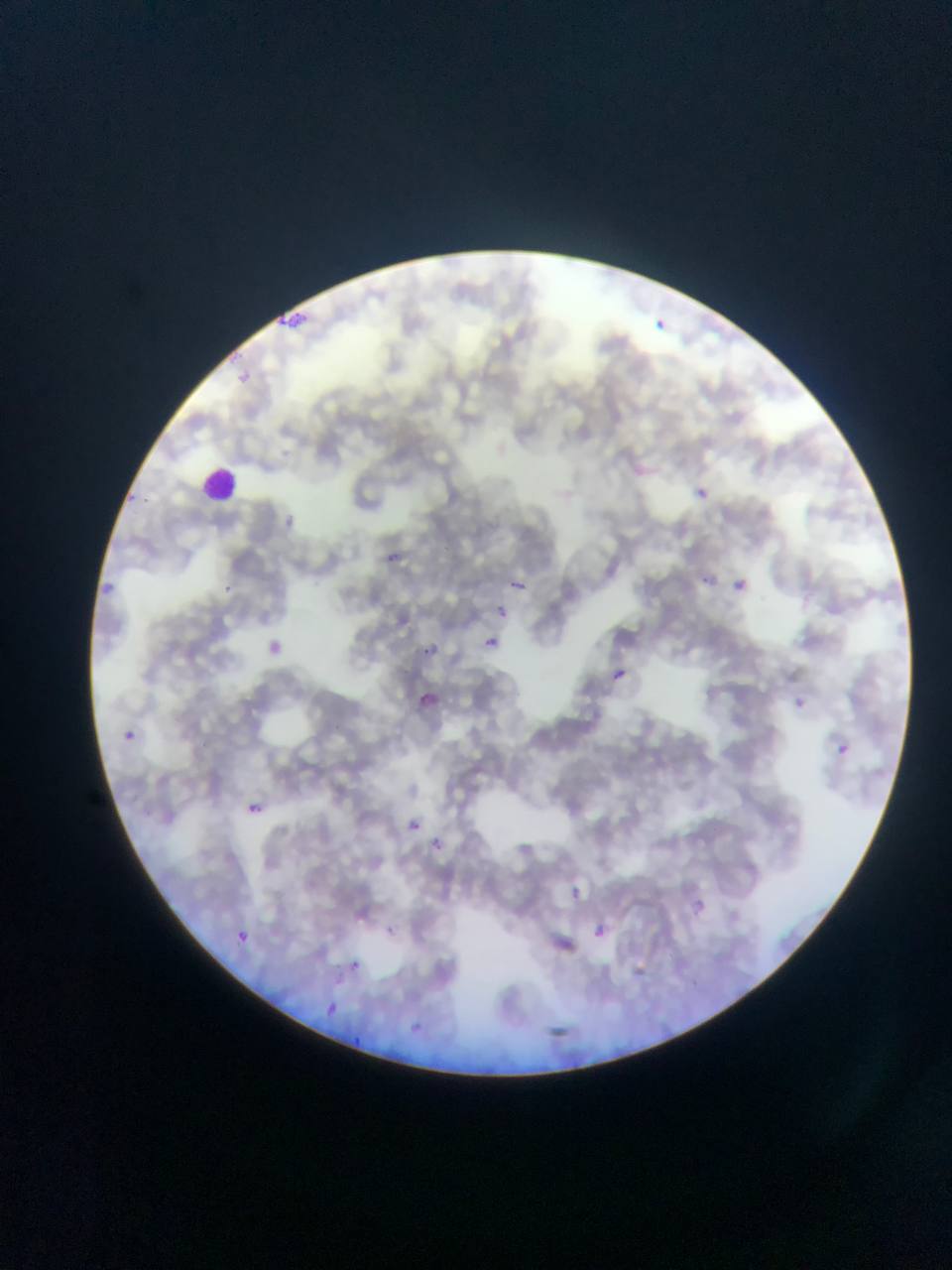

Approximate bounding boxes as [left, top, right, bottom] in pixels.
Summary:
  - Plasmodium parasite locations: [271, 309, 311, 338], [655, 316, 669, 330], [231, 368, 254, 391], [632, 458, 649, 478], [124, 486, 144, 500], [694, 486, 710, 502], [286, 503, 300, 538], [375, 545, 414, 568], [701, 574, 714, 586], [502, 576, 538, 602], [733, 578, 748, 592], [96, 579, 116, 597], [492, 604, 520, 625], [481, 635, 513, 665], [269, 636, 293, 658], [421, 641, 453, 665], [614, 669, 626, 681], [413, 689, 442, 707], [125, 730, 137, 743], [837, 743, 850, 756], [247, 803, 261, 815], [396, 812, 422, 837], [428, 832, 448, 862], [564, 880, 588, 910], [690, 899, 706, 917], [592, 918, 613, 941], [229, 929, 257, 946], [549, 931, 577, 963], [349, 960, 361, 971], [322, 999, 341, 1019], [407, 1019, 418, 1033], [545, 1024, 576, 1041], [349, 1033, 367, 1046]
  - Leukocyte locations: [202, 467, 242, 503]
  - Preparation: thin blood film
  - Capture: mobile-phone photograph through a microscope
  - Country: Ghana
  - Image size: 952×1270 pixels
  - Field of view: single